Describe the morphology of the red blood cells.
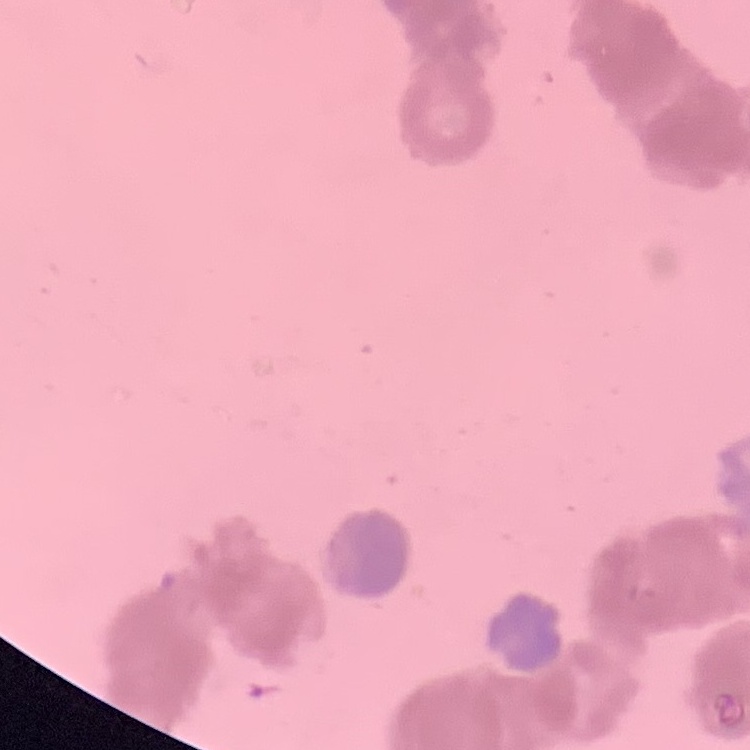
They show rouleaux formation.

stain = Field's or Giemsa
preparation = thin peripheral smear
image type = one tile cut from a larger photomicrograph